Name the parasite shown.
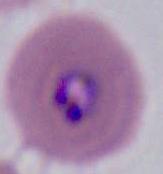
This is Plasmodium.

modality = photomicrograph
magnification = 400x or 1000x